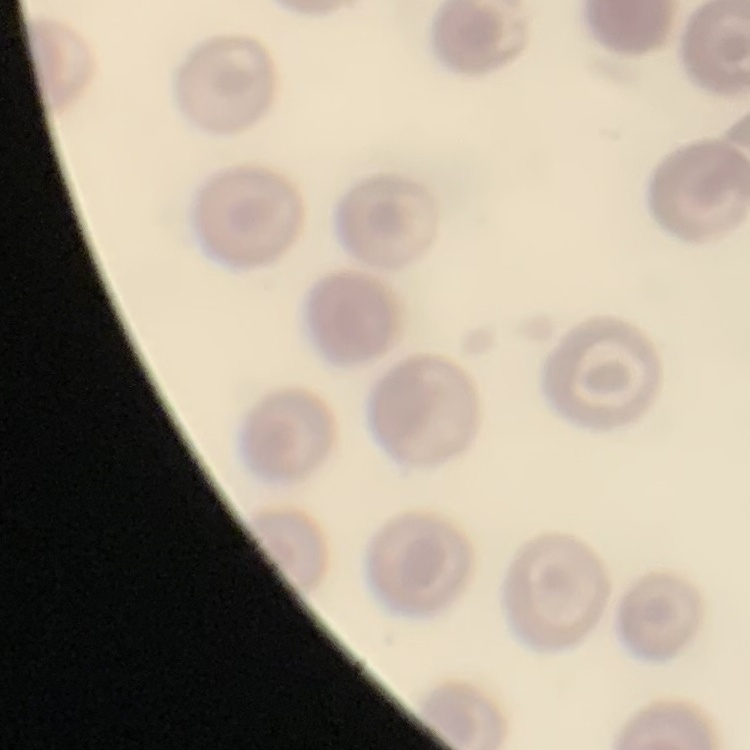

The red blood cells show no rouleaux formation. Stained with either Field's or Giemsa. One tile cut from a larger photomicrograph. Thin blood film.